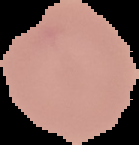
Summary:
  - Image type: cell region segmented out of the field of view; surrounding area masked to black
  - Result: no Plasmodium parasites detected
  - Image size: 139×145 pixels
  - Preparation: thin blood film